Report the malaria status of this cell.
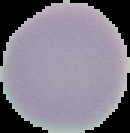

Uninfected.

Summary:
  - Preparation: thin blood smear
  - Image type: segmented cell region on a black background
  - Image size: 130×133 pixels